Report the malaria status of this cell.
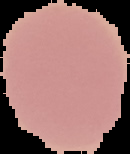

Uninfected.

image size = 130×154 pixels
preparation = thin blood smear
image type = segmented cell region on a black background